State which parasite is depicted.
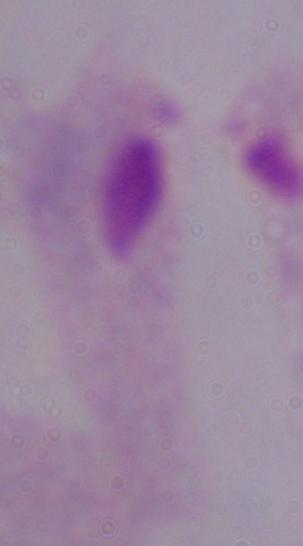
This is a trichomonad.

1000x magnification. Micrograph.